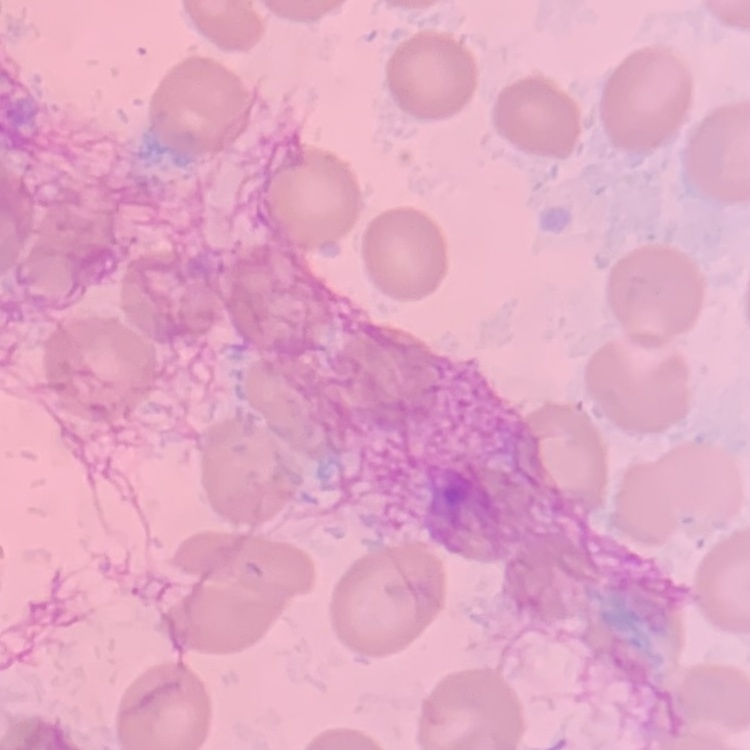

Summary:
  - Erythrocyte morphology: no rouleaux formation
  - Image type: square crop of a larger photomicrograph
  - Preparation: thin blood film
  - Stain: Field's or Giemsa